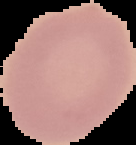

image_type: cell region segmented out of the field of view; surrounding area masked to black
result: no malaria parasites detected
image_size: 136×145 pixels
preparation: thin blood film